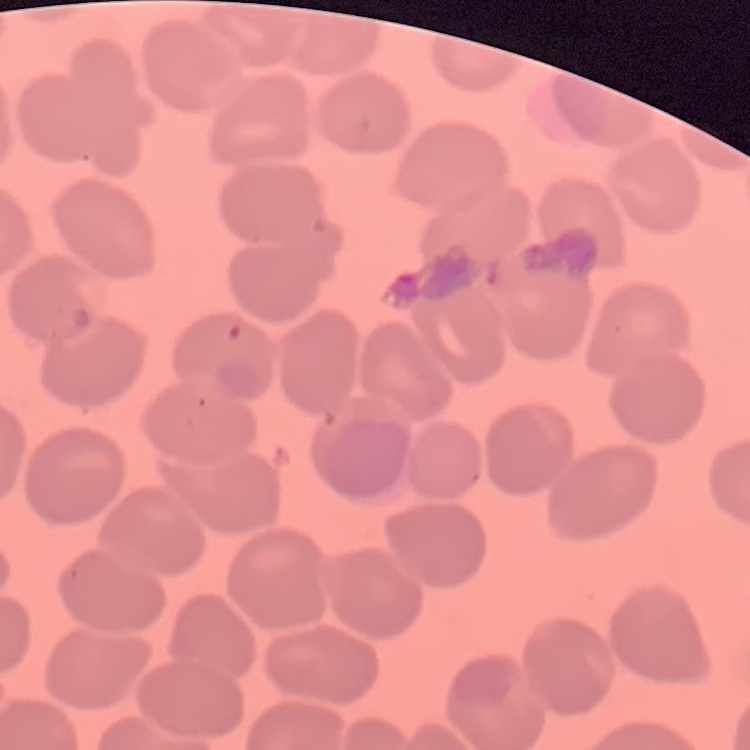 The red blood cells show no rouleaux formation. Field's or Giemsa stain. Thin blood smear. One tile cut from a larger photomicrograph.